Comment on the morphology of the erythrocytes.
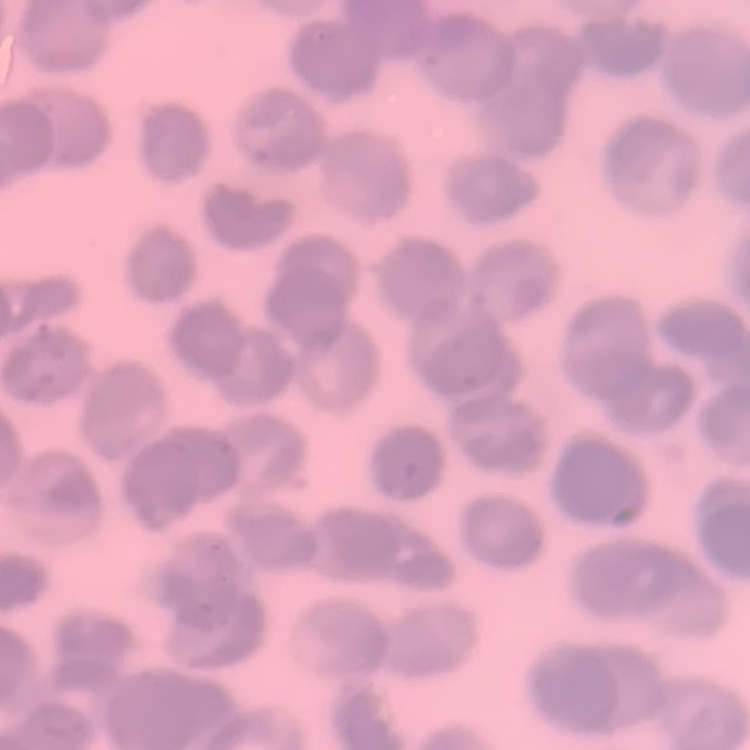

Rouleaux formation.

preparation: thin peripheral smear
stain: Field's or Giemsa
image_type: one tile cut from a larger photomicrograph